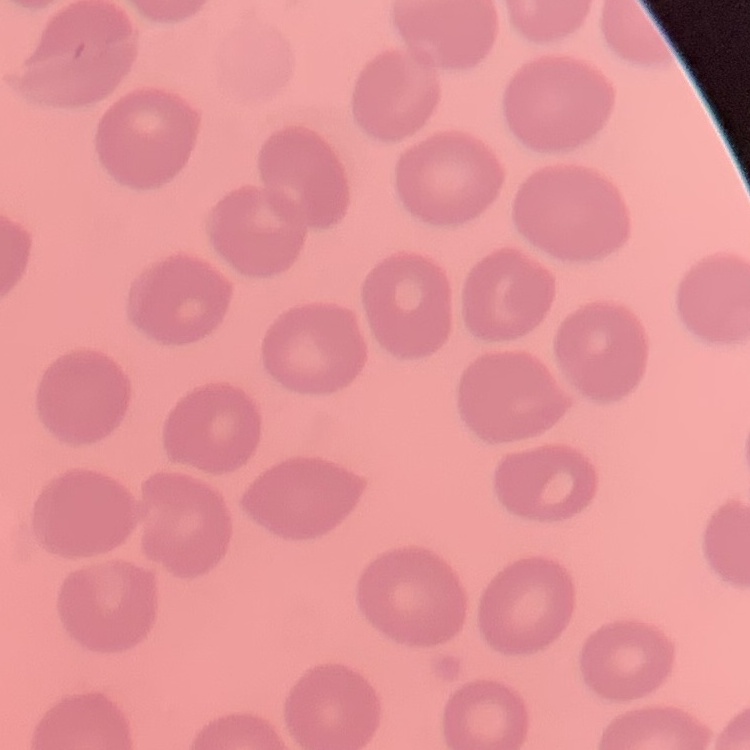

Summary:
  - Erythrocyte morphology: no rouleaux formation
  - Stain: Field's or Giemsa
  - Image type: one tile cut from a larger photomicrograph
  - Preparation: thin blood film